Assess this cell for malaria.
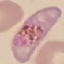

Parasitized.

Giemsa stain. Cell patch, automatically extracted from a larger field of view and resized to 64 × 64 pixels. Thin blood smear. Photographed with a smartphone camera at the microscope eyepiece.